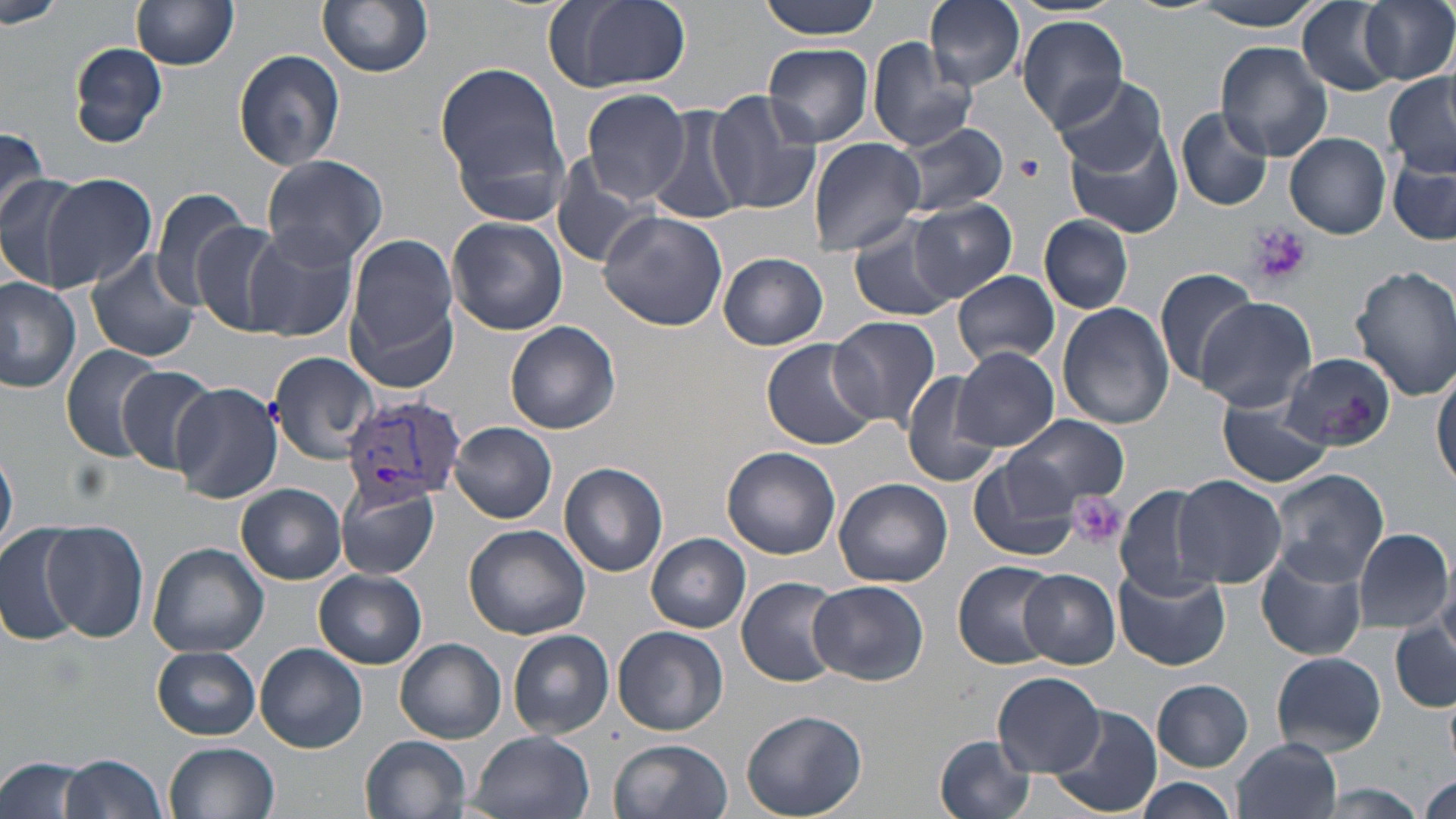
{
  "slide_level_diagnosis": "Plasmodium vivax",
  "preparation": "thin blood smear",
  "field_of_view": "one of a larger specimen",
  "magnification": "1000x",
  "image_size": "1456×819 pixels",
  "platelet_locations": "approximate bounding boxes as (x1, y1, x2, y2) in pixels: (1017, 152, 1046, 181), (1245, 223, 1312, 287), (1071, 494, 1126, 549)",
  "stain": "May-Grünwald-Giemsa",
  "modality": "light microscopy",
  "plasmodium_vivax_infected_red_blood_cell_locations": "approximate bounding boxes as (x1, y1, x2, y2) in pixels: (345, 397, 468, 503)",
  "uninfected_red_blood_cell_locations": "approximate bounding boxes as (x1, y1, x2, y2) in pixels: (130, 0, 240, 70), (317, 0, 434, 78), (542, 0, 693, 97), (758, 0, 881, 39), (925, 0, 1025, 90), (1124, 0, 1224, 16), (1190, 0, 1326, 31), (1359, 0, 1456, 85), (0, 1, 66, 28), (1296, 2, 1399, 97), (1016, 14, 1130, 132), (866, 37, 977, 151), (69, 41, 170, 148), (763, 41, 874, 148), (1215, 42, 1335, 163), (233, 47, 345, 172), (438, 63, 569, 201), (1051, 74, 1167, 177), (1383, 74, 1456, 177), (579, 90, 690, 203), (705, 91, 823, 216), (650, 106, 749, 227), (1177, 107, 1273, 211), (893, 121, 1009, 217), (1064, 127, 1185, 239), (0, 128, 51, 227), (1285, 133, 1391, 238), (807, 137, 926, 256), (553, 152, 661, 271), (260, 154, 390, 269), (1388, 156, 1455, 247), (40, 173, 158, 290), (0, 175, 86, 289), (148, 188, 257, 308), (910, 198, 1016, 300), (598, 210, 729, 331), (1039, 214, 1133, 314), (448, 217, 567, 335), (849, 218, 958, 322), (190, 220, 286, 332), (244, 226, 359, 342), (345, 235, 463, 374), (86, 250, 202, 364), (717, 252, 829, 349), (1348, 265, 1456, 399), (1152, 266, 1259, 388), (952, 270, 1060, 366), (0, 277, 81, 391), (1195, 297, 1317, 413), (1057, 302, 1175, 430), (828, 317, 941, 429), (506, 322, 621, 434), (761, 339, 880, 451), (61, 343, 167, 461), (953, 346, 1059, 450), (267, 350, 382, 463), (1282, 352, 1396, 449), (114, 366, 221, 476), (1433, 370, 1456, 490), (900, 372, 1002, 490), (172, 382, 285, 503), (1216, 398, 1333, 488), (1003, 414, 1128, 509), (451, 422, 556, 524), (1, 443, 17, 559), (722, 447, 841, 560), (968, 456, 1082, 562), (559, 462, 668, 577), (1266, 469, 1388, 585), (1174, 475, 1286, 587), (834, 476, 953, 587), (336, 480, 440, 581), (237, 483, 348, 583), (1114, 483, 1221, 601), (39, 522, 148, 643), (0, 524, 88, 646), (465, 525, 591, 641), (1354, 528, 1452, 631), (647, 533, 751, 633), (148, 542, 269, 657), (1256, 548, 1367, 662), (952, 560, 1061, 669), (1111, 565, 1231, 671), (314, 569, 427, 669), (1018, 570, 1120, 668), (736, 576, 846, 687), (809, 580, 928, 685), (1390, 618, 1455, 710), (613, 625, 728, 736), (508, 629, 614, 738), (395, 637, 507, 744), (256, 643, 368, 754), (152, 645, 261, 739), (1272, 652, 1386, 754), (993, 672, 1103, 775), (1152, 678, 1253, 772), (1445, 691, 1456, 773), (1046, 704, 1162, 816), (740, 709, 866, 819), (471, 730, 595, 819), (361, 735, 471, 819), (934, 735, 1036, 819), (609, 738, 731, 819), (1231, 738, 1343, 819), (164, 742, 279, 819), (0, 753, 90, 819), (59, 753, 168, 819), (1420, 773, 1455, 819), (1133, 778, 1238, 819)"
}